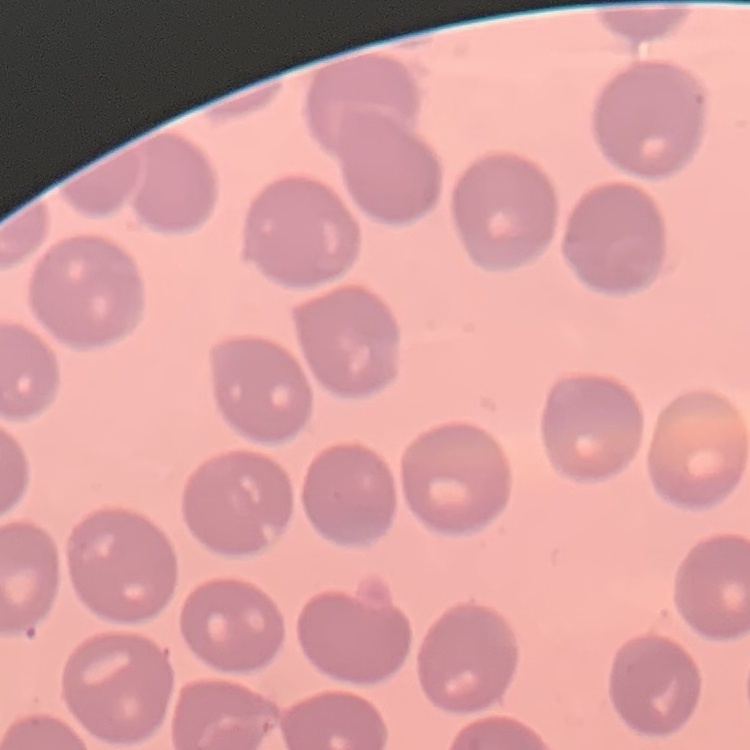

Summary:
  - Erythrocyte morphology: no rouleaux formation
  - Image type: one tile cut from a larger photomicrograph
  - Preparation: thin blood film
  - Stain: Field's or Giemsa